Mark where platelets are.
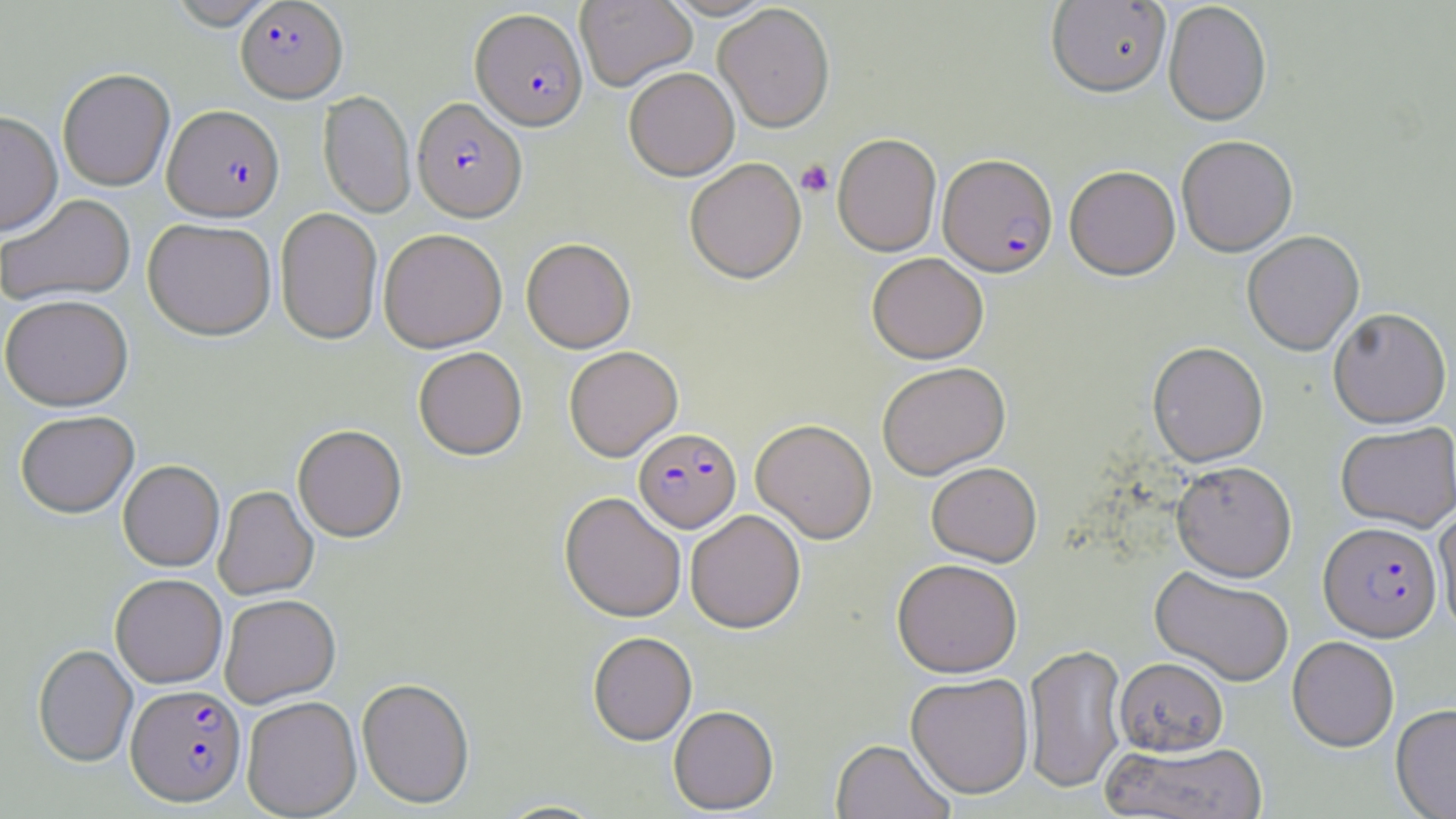
Approximate bounding boxes as [x1, y1, x2, y2] in pixels.
Platelets: [796, 159, 834, 197].

Plasmodium falciparum-infected red blood cell locations: [235, 0, 347, 102], [471, 8, 588, 131], [412, 98, 527, 222], [163, 105, 284, 221], [938, 154, 1058, 278], [634, 428, 741, 533], [1318, 523, 1441, 643], [125, 686, 246, 807]. Uninfected red blood cell locations: [575, 0, 697, 91], [1046, 0, 1171, 98], [165, 1, 279, 29], [1163, 2, 1272, 126], [714, 4, 835, 133], [624, 67, 739, 181], [57, 68, 175, 191], [318, 91, 415, 218], [0, 111, 62, 235], [833, 134, 941, 257], [1177, 136, 1297, 257], [684, 159, 806, 285], [1064, 165, 1180, 280], [0, 193, 136, 307], [274, 208, 383, 345], [143, 218, 277, 341], [379, 229, 507, 352], [1242, 232, 1365, 356], [521, 239, 636, 353], [867, 253, 988, 364], [0, 294, 133, 411], [1328, 310, 1452, 430], [1147, 342, 1269, 468], [563, 346, 683, 462], [413, 347, 527, 461], [877, 362, 1011, 480], [15, 411, 139, 518], [750, 419, 877, 544], [1336, 424, 1456, 533], [293, 425, 407, 543], [118, 460, 224, 572], [1171, 461, 1297, 583], [926, 462, 1042, 567], [213, 486, 318, 600], [559, 492, 686, 624], [1434, 506, 1456, 637], [686, 511, 806, 633], [892, 560, 1022, 679], [1150, 567, 1293, 687], [110, 574, 227, 688], [219, 594, 341, 708], [587, 632, 697, 746], [1287, 638, 1399, 753], [33, 644, 138, 768], [1024, 645, 1127, 794], [1114, 658, 1229, 757], [905, 674, 1035, 801], [356, 678, 475, 809], [242, 697, 362, 818], [1391, 704, 1456, 819], [668, 706, 779, 816], [831, 740, 954, 819], [1103, 741, 1271, 819], [495, 800, 608, 818]. Slide-level diagnosis: Plasmodium falciparum. Thin blood film. May-Grünwald-Giemsa-stained preparation. Image is 1456×819 pixels. Light microscopy. One field of a larger specimen. Captured at 1000x magnification.